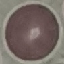

Malaria status: uninfected. Automatically extracted cell patch, resized to 64 × 64 pixels. Giemsa stain. Acquired by smartphone through the microscope eyepiece. Thin smear of blood.